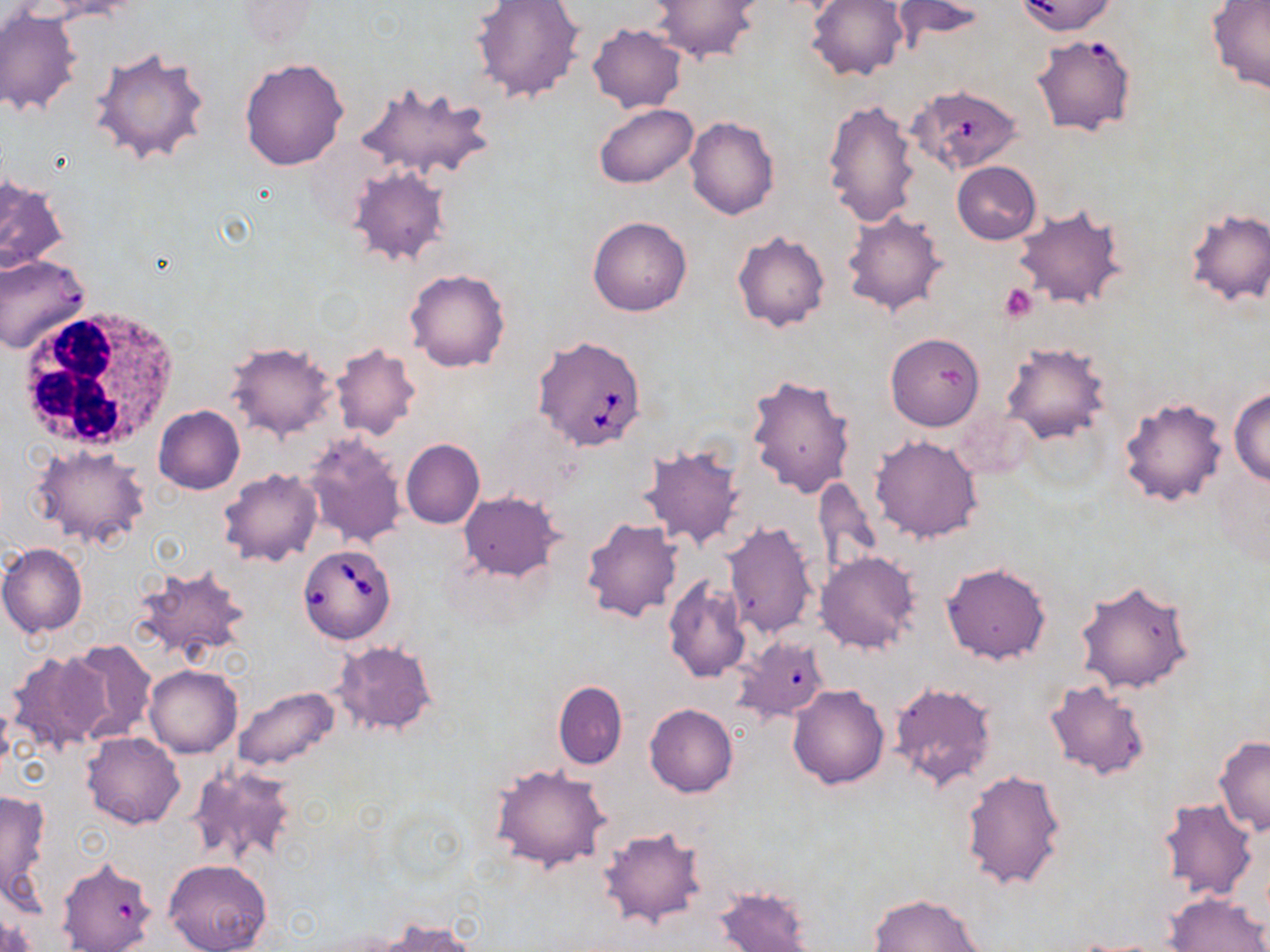
{
  "babesia_divergens_infected_red_blood_cell_locations": "approximate bounding boxes as (x1,y1)-(x2,y2) corner pairs in pixels: (910,83)-(1025,175), (533,334)-(648,453), (298,543)-(398,644)",
  "slide_level_diagnosis": "Babesia divergens",
  "preparation": "thin blood smear",
  "uninfected_red_blood_cell_locations": "approximate bounding boxes as (x1,y1)-(x2,y2) corner pairs in pixels: (469,0)-(586,104), (806,0)-(907,83), (891,0)-(987,47), (1013,0)-(1120,36), (649,1)-(760,63), (1205,1)-(1270,96), (1,8)-(84,117), (587,22)-(686,113), (1038,38)-(1136,144), (89,46)-(210,166), (239,58)-(349,171), (353,80)-(495,187), (823,97)-(920,226), (592,104)-(698,188), (685,117)-(780,220), (952,161)-(1041,245), (347,166)-(451,267), (0,175)-(70,274), (1012,206)-(1129,310), (1183,207)-(1269,307), (840,209)-(950,318), (587,215)-(692,317), (732,231)-(830,332), (0,255)-(89,354), (404,268)-(510,372), (885,332)-(984,430), (226,340)-(338,441), (1002,341)-(1111,442), (329,342)-(421,441), (747,372)-(856,499), (1231,387)-(1270,486), (1117,395)-(1229,509), (153,404)-(245,494), (301,433)-(407,549), (869,434)-(984,543), (400,439)-(484,529), (638,443)-(746,550), (31,445)-(151,550), (218,469)-(324,567), (811,476)-(882,581), (459,491)-(565,581), (581,519)-(681,622), (722,521)-(819,639), (0,544)-(88,637), (815,551)-(920,655), (940,562)-(1051,665), (131,563)-(252,664), (663,578)-(753,684), (1072,578)-(1195,695), (733,635)-(828,726), (62,640)-(157,744), (331,640)-(438,738), (6,650)-(110,754), (145,664)-(242,757), (1044,678)-(1151,780), (553,681)-(627,769), (889,681)-(999,792), (787,684)-(889,789), (231,685)-(340,772), (645,704)-(738,797), (82,732)-(185,829), (1214,737)-(1270,837), (187,764)-(298,866), (489,764)-(611,873), (959,769)-(1067,893), (0,788)-(52,901), (1158,797)-(1258,901), (598,827)-(709,929), (164,859)-(272,952), (53,860)-(154,951), (714,886)-(815,952), (1163,891)-(1270,952), (867,893)-(987,952), (374,919)-(478,951)",
  "magnification": "1000x",
  "modality": "optical microscopy",
  "field_of_view": "single",
  "platelet_locations": "approximate bounding boxes as (x1,y1)-(x2,y2) corner pairs in pixels: (1000,284)-(1037,322)",
  "stain": "May-Grünwald-Giemsa",
  "image_size": "1270×952 pixels",
  "white_blood_cell_locations": "approximate bounding boxes as (x1,y1)-(x2,y2) corner pairs in pixels: (14,304)-(178,457)"
}